Report the malaria status of this cell.
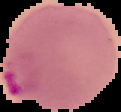

Parasitized.

{
  "preparation": "thin blood film",
  "image_type": "cell region segmented out of the field of view; surrounding area masked to black",
  "image_size": "121×112 pixels"
}